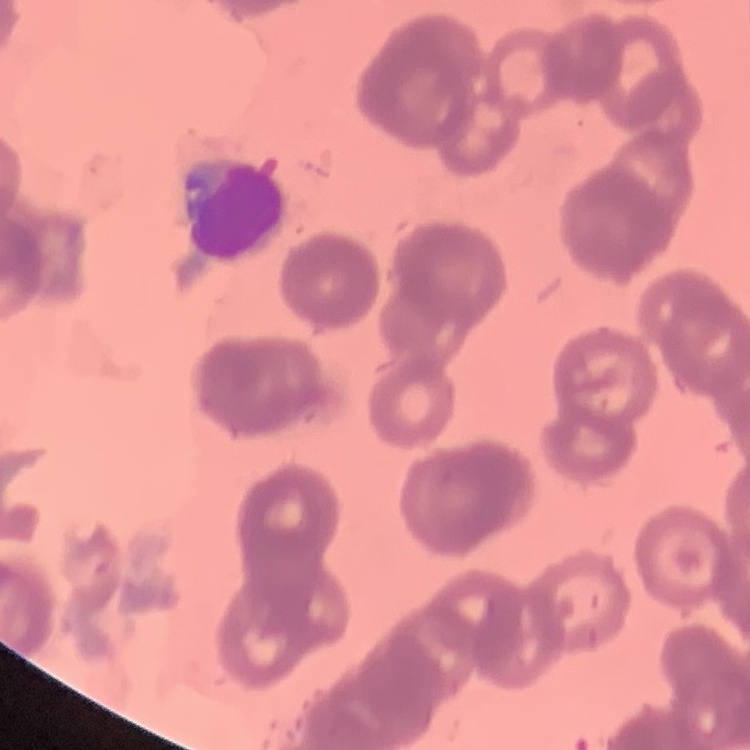

{
  "red_blood_cell_morphology": "rouleaux formation",
  "stain": "Field's or Giemsa",
  "preparation": "thin blood film",
  "image_type": "one tile cut from a larger photomicrograph"
}